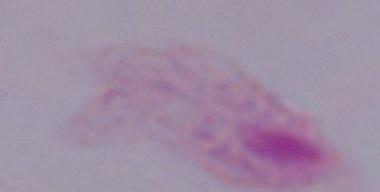
Summary:
  - Identification: trichomonad
  - Magnification: 1000x
  - Modality: micrograph